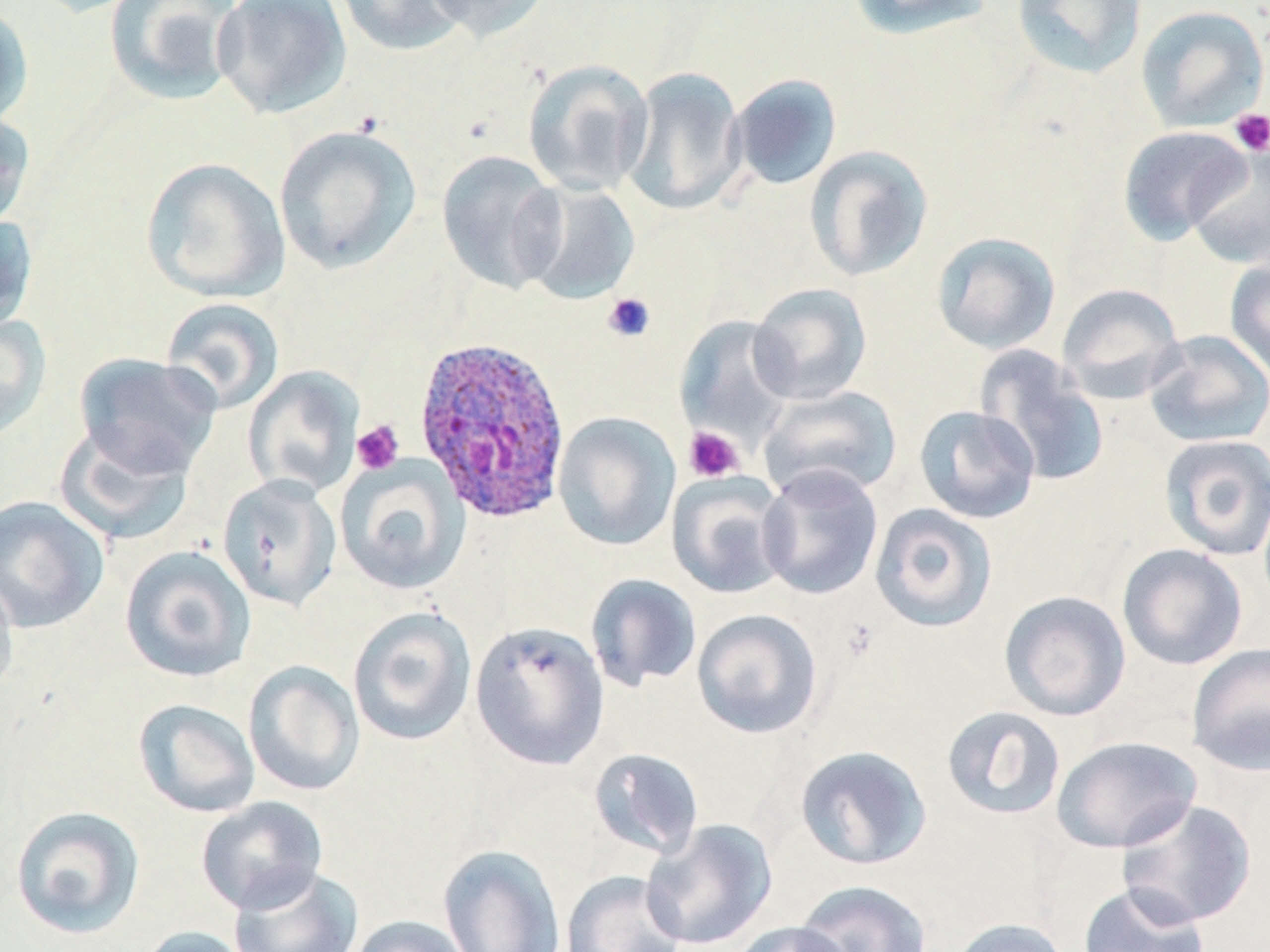

Summary:
  - Coordinate format: approximate bounding boxes as named x1/y1/x2/y2 corners in pixels
  - Uninfected red blood cell locations: (x1=103, y1=0, x2=244, y2=106), (x1=212, y1=0, x2=352, y2=119), (x1=333, y1=0, x2=469, y2=57), (x1=423, y1=0, x2=552, y2=43), (x1=848, y1=0, x2=994, y2=40), (x1=1011, y1=0, x2=1147, y2=79), (x1=0, y1=3, x2=33, y2=129), (x1=1135, y1=4, x2=1269, y2=132), (x1=522, y1=59, x2=654, y2=195), (x1=622, y1=66, x2=747, y2=215), (x1=728, y1=73, x2=842, y2=191), (x1=0, y1=108, x2=35, y2=232), (x1=274, y1=124, x2=421, y2=274), (x1=1117, y1=125, x2=1251, y2=245), (x1=1186, y1=142, x2=1270, y2=269), (x1=804, y1=144, x2=934, y2=282), (x1=437, y1=150, x2=566, y2=294), (x1=141, y1=157, x2=290, y2=302), (x1=518, y1=182, x2=641, y2=305), (x1=0, y1=211, x2=37, y2=333), (x1=931, y1=231, x2=1061, y2=355), (x1=1224, y1=256, x2=1270, y2=379), (x1=747, y1=282, x2=872, y2=405), (x1=1056, y1=283, x2=1186, y2=403), (x1=160, y1=297, x2=284, y2=415), (x1=0, y1=313, x2=52, y2=442), (x1=674, y1=315, x2=797, y2=448), (x1=1144, y1=330, x2=1270, y2=448), (x1=976, y1=347, x2=1109, y2=487), (x1=73, y1=352, x2=221, y2=479), (x1=243, y1=366, x2=364, y2=498), (x1=758, y1=385, x2=902, y2=502), (x1=914, y1=404, x2=1041, y2=524), (x1=553, y1=412, x2=681, y2=551), (x1=53, y1=423, x2=196, y2=545), (x1=1158, y1=434, x2=1270, y2=561), (x1=335, y1=456, x2=470, y2=595), (x1=757, y1=464, x2=884, y2=600), (x1=666, y1=472, x2=792, y2=600), (x1=217, y1=474, x2=342, y2=610), (x1=0, y1=495, x2=109, y2=633), (x1=869, y1=503, x2=999, y2=632), (x1=1117, y1=543, x2=1248, y2=670), (x1=120, y1=545, x2=257, y2=683), (x1=585, y1=573, x2=702, y2=691), (x1=0, y1=575, x2=19, y2=702), (x1=999, y1=590, x2=1131, y2=722), (x1=348, y1=605, x2=477, y2=746), (x1=691, y1=608, x2=823, y2=739), (x1=470, y1=620, x2=610, y2=770), (x1=1186, y1=643, x2=1270, y2=776), (x1=243, y1=660, x2=365, y2=797), (x1=132, y1=698, x2=260, y2=818), (x1=941, y1=705, x2=1066, y2=821), (x1=1052, y1=735, x2=1202, y2=853), (x1=793, y1=744, x2=932, y2=870), (x1=588, y1=747, x2=705, y2=859), (x1=195, y1=796, x2=329, y2=915), (x1=1116, y1=799, x2=1257, y2=928), (x1=10, y1=805, x2=145, y2=939), (x1=641, y1=818, x2=778, y2=950), (x1=437, y1=844, x2=566, y2=951), (x1=228, y1=865, x2=364, y2=951), (x1=561, y1=870, x2=686, y2=952), (x1=795, y1=879, x2=932, y2=951), (x1=1077, y1=882, x2=1210, y2=952), (x1=347, y1=915, x2=473, y2=952), (x1=947, y1=917, x2=1071, y2=952), (x1=731, y1=920, x2=854, y2=952), (x1=135, y1=926, x2=255, y2=952)
  - Platelet locations: (x1=1229, y1=108, x2=1270, y2=156), (x1=602, y1=292, x2=656, y2=343), (x1=351, y1=421, x2=404, y2=475), (x1=684, y1=426, x2=745, y2=482)
  - Plasmodium ovale-infected red blood cell locations: (x1=414, y1=334, x2=572, y2=524)
  - Slide-level diagnosis: Plasmodium ovale
  - Stain: May-Grünwald-Giemsa
  - Modality: light microscopy
  - Magnification: 1000x
  - Field of view: one of a larger specimen
  - Image size: 1270×952 pixels
  - Preparation: thin blood film